State which parasite is depicted.
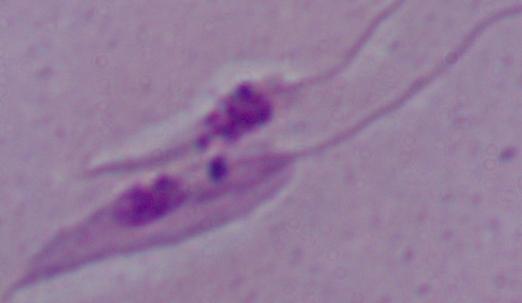

Leishmania.

Summary:
  - Magnification: 1000x
  - Modality: photomicrograph